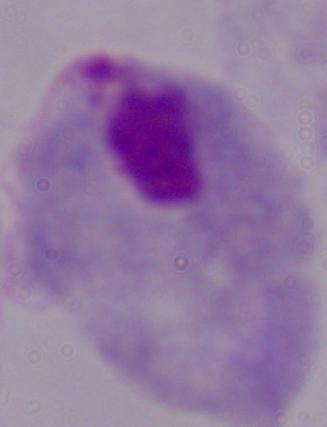
A trichomonad is shown. Micrograph. 1000x magnification.